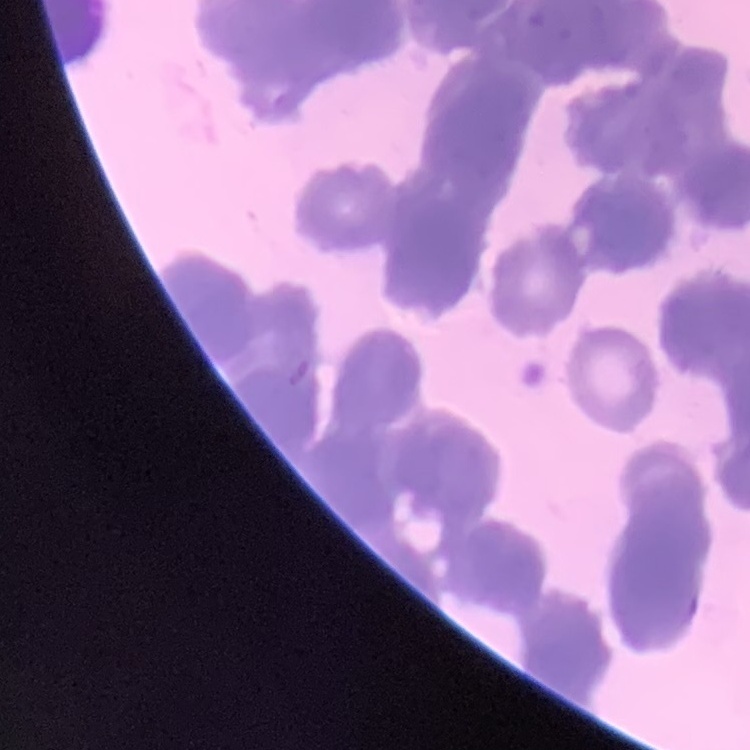
Summary:
  - Red blood cell morphology: rouleaux formation
  - Preparation: thin peripheral smear
  - Stain: Field's or Giemsa
  - Image type: one tile cut from a larger photomicrograph